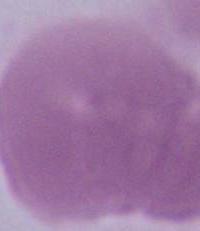

Photomicrograph. Captured at 1000x magnification. An erythrocyte is seen.